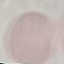

Malaria status: uninfected. Thin smear of blood. Photographed with a smartphone camera at the microscope eyepiece. Giemsa stain. Automatically extracted cell patch, resized to 64 × 64 pixels.